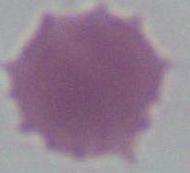
{
  "modality": "micrograph",
  "magnification": "1000x",
  "identification": "red blood cell"
}